Assess this cell for malaria.
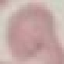

It is uninfected.

capture: smartphone through the microscope eyepiece
preparation: thin blood film
stain: Giemsa
image_type: automatically extracted cell patch, resized to 64 × 64 pixels